State the preparation type.
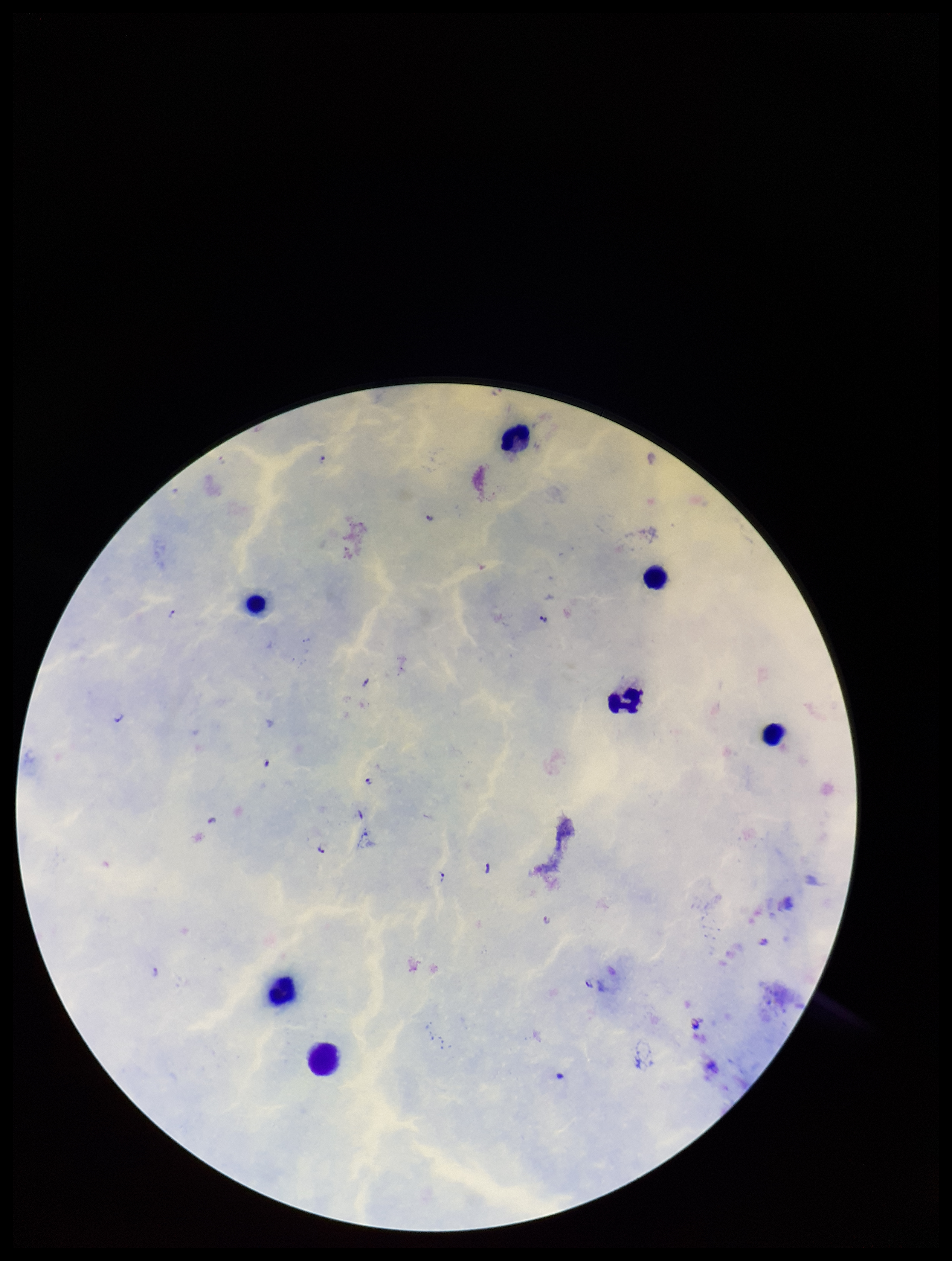
A thick smear.

Patient malaria status: infected. Single field of view. Smartphone photograph taken through the eyepiece of a microscope. Leukocyte count: 7. Species reported for this patient: Plasmodium falciparum. Giemsa stain. Plasmodium parasites: identified. Image is 952×1261 pixels. Parasite count: 13.